Locate every Plasmodium parasite and every leukocyte.
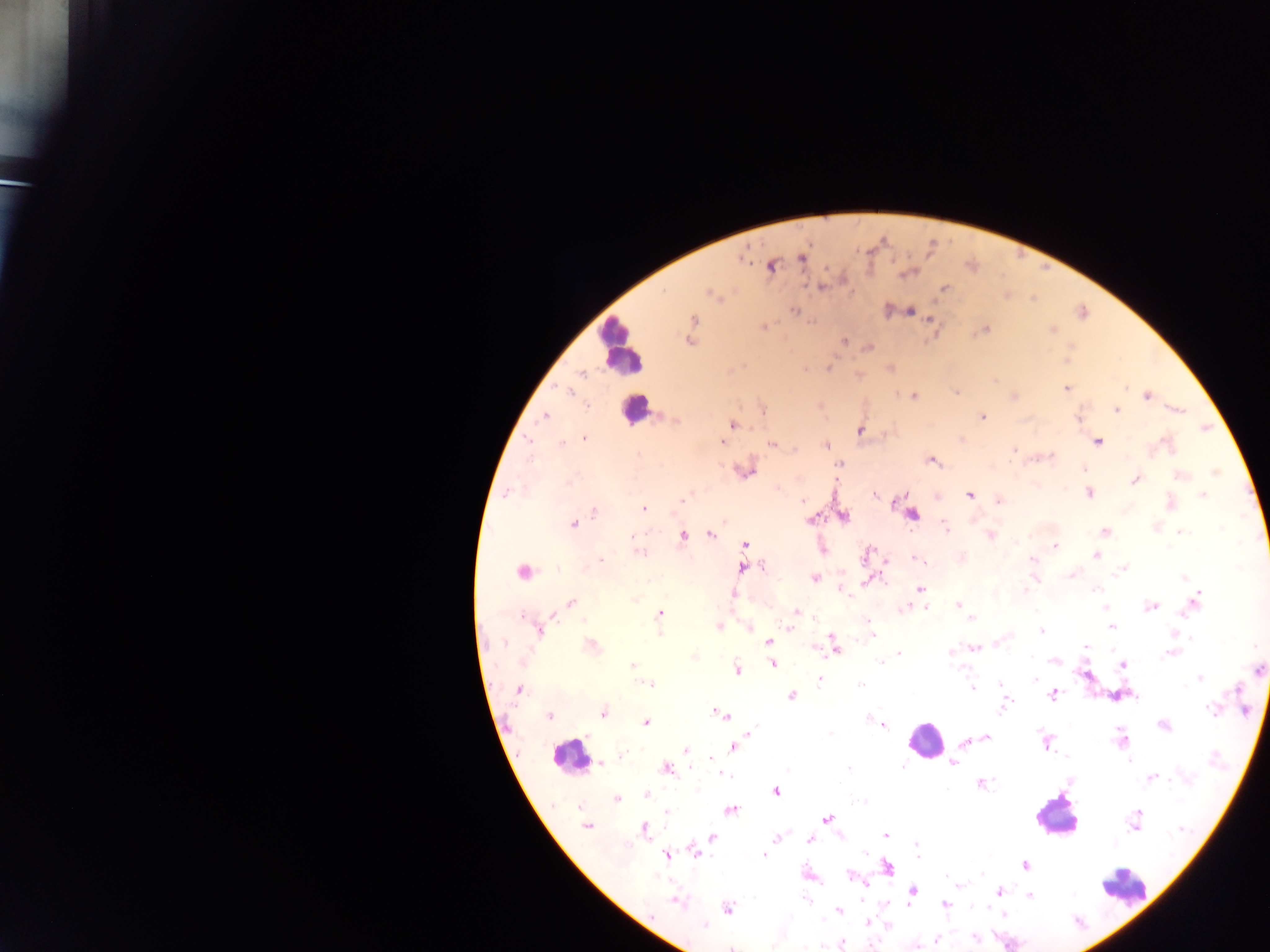
Approximate centers as x y in pixels.
Plasmodium parasites: 802 256; 743 257; 770 266; 906 272; 822 287; 944 288; 712 294; 794 310; 888 310; 907 311; 693 319; 931 320; 763 326; 691 327; 984 329; 1051 329; 690 340; 844 341; 868 347; 1066 360; 889 368; 805 369; 857 376; 1066 387; 955 391; 913 396; 1012 396; 1146 396; 821 406; 762 408; 1114 409; 1176 410; 545 415; 982 417; 1078 417; 733 424; 859 429; 583 438; 961 439; 721 441; 1097 442; 559 444; 771 444; 825 444; 1013 448; 638 455; 1048 457; 930 459; 839 464; 744 469; 1083 469; 1215 470; 1179 476; 1135 478; 1089 492; 505 493; 969 494; 938 495; 1202 495; 902 498; 1000 500; 803 501; 1169 503; 643 509; 594 512; 910 512; 842 515; 811 519; 573 524; 1155 527; 1104 532; 1179 532; 711 534; 990 534; 683 536; 744 544; 1054 547; 822 548; 639 551; 870 551; 1096 555; 918 558; 961 559; 600 560; 886 560; 1031 560; 761 566; 743 567; 1121 570; 522 571; 1072 574; 814 577; 1034 577; 868 579; 841 589; 919 589; 1025 592; 734 594; 635 599; 1195 601; 571 603; 958 605; 1151 606; 925 607; 1106 607; 905 608; 796 612; 659 614; 972 618; 718 626; 868 626; 1111 626; 749 627; 539 628; 789 628; 1041 630; 768 642; 590 645; 834 646; 972 646; 1085 646; 813 647; 1172 653; 899 654; 950 654; 693 655; 1053 659; 772 663; 1122 664; 632 665; 737 669; 1258 669; 1086 673; 819 678; 1200 678; 651 684; 1002 686; 971 688; 519 689; 1053 694; 1119 694; 790 695; 1004 704; 716 711; 603 713; 722 714; 549 715; 646 723; 883 724; 1163 725; 985 736; 1122 739; 966 741; 1045 742; 733 747; 686 749; 621 756; 712 758; 600 763; 952 763; 665 767; 719 773; 1150 777; 980 783; 775 790; 646 795; 617 798; 730 810; 667 813; 826 818; 1135 823; 587 826; 644 828; 885 835; 711 837; 777 838; 810 838; 917 845; 695 851; 764 853; 667 854; 1025 865; 887 866; 808 875; 852 877; 862 883; 957 884; 912 890; 999 891; 1029 894; 675 900; 945 904; 727 908; 838 910; 1003 915; 868 923; 886 924; 974 938; 934 939; 839 943; 732 946.
Leukocytes: 621 346; 634 408; 925 740; 570 755; 1056 815; 1123 886.

Thick blood film. Mobile-phone photograph taken through the microscope. Image is 1270×952 pixels. Single field of view. Collected in Ghana.